Name the cell type shown.
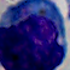

This is a leukocyte.

Summary:
  - Modality: micrograph
  - Magnification: 1000x